Outline each uninfected red blood cell.
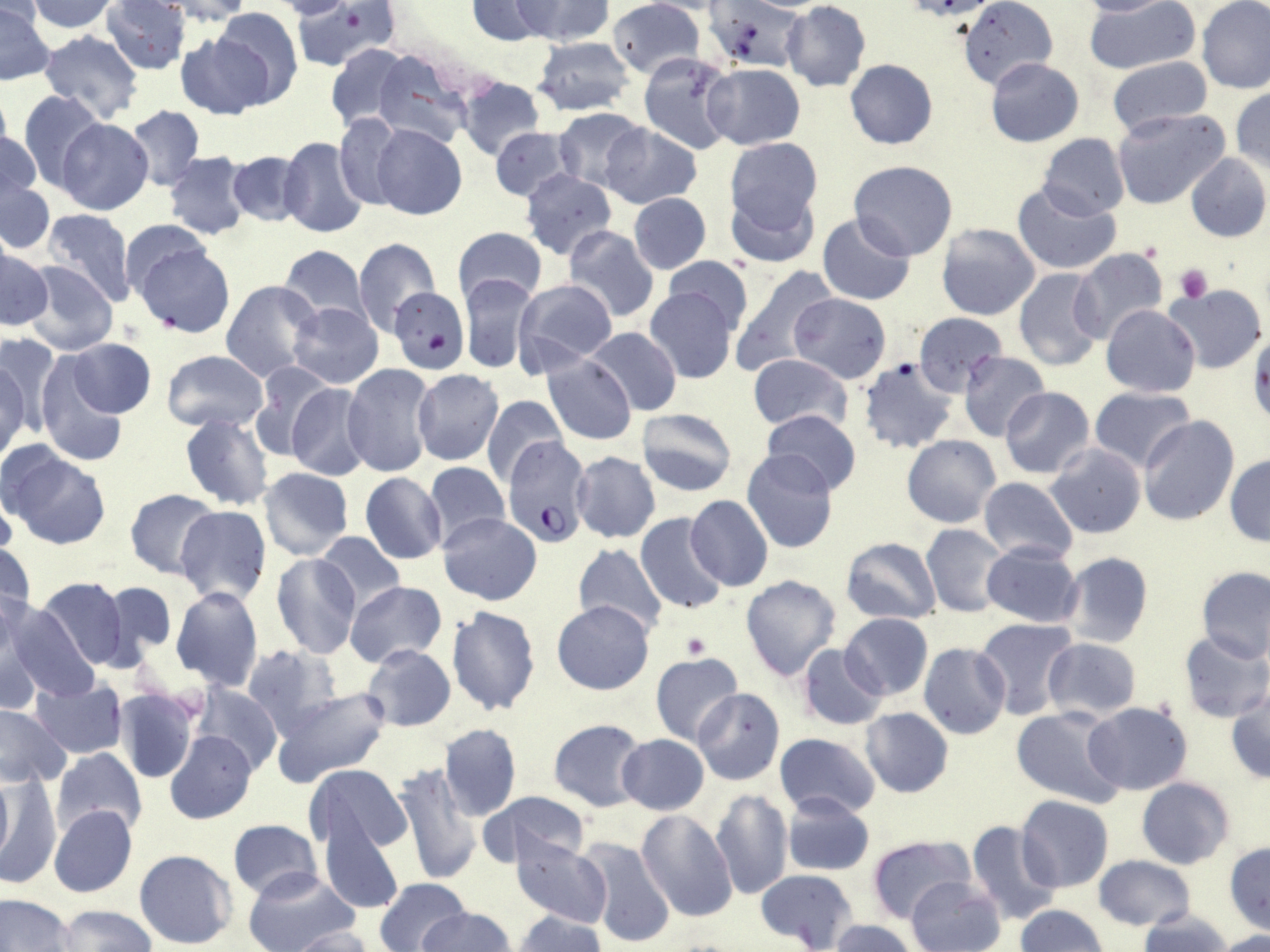
Approximate bounding boxes as (x1, y1, x2, y2) in pixels.
Uninfected red blood cells: (26, 0, 119, 35), (103, 0, 190, 74), (159, 0, 253, 25), (272, 0, 351, 20), (293, 0, 395, 72), (467, 0, 554, 45), (512, 0, 614, 45), (608, 0, 704, 78), (960, 0, 1058, 88), (1076, 0, 1171, 16), (1085, 0, 1201, 75), (1197, 0, 1270, 93), (782, 1, 871, 92), (712, 2, 804, 71), (0, 3, 54, 85), (214, 8, 303, 106), (38, 29, 145, 123), (174, 29, 274, 119), (532, 37, 636, 116), (326, 44, 412, 131), (373, 51, 477, 149), (638, 51, 737, 154), (1105, 55, 1212, 134), (985, 57, 1084, 147), (846, 59, 937, 149), (703, 64, 806, 149), (457, 77, 545, 160), (0, 86, 14, 168), (1230, 88, 1270, 176), (18, 89, 105, 189), (126, 106, 205, 191), (554, 107, 649, 194), (1112, 108, 1231, 211), (334, 115, 408, 211), (55, 117, 153, 214), (371, 123, 466, 220), (601, 124, 702, 208), (488, 126, 575, 201), (1, 129, 40, 203), (1038, 134, 1130, 219), (278, 135, 371, 239), (723, 136, 825, 242), (226, 150, 307, 226), (164, 152, 252, 237), (1185, 153, 1270, 242), (850, 161, 958, 260), (521, 170, 616, 258), (0, 179, 55, 254), (724, 180, 821, 270), (1012, 180, 1123, 275), (629, 193, 711, 273), (43, 209, 136, 305), (817, 212, 916, 305), (120, 219, 210, 302), (936, 222, 1040, 320), (563, 226, 659, 323), (453, 227, 547, 306), (353, 237, 440, 335), (135, 241, 235, 335), (278, 245, 370, 327), (1069, 247, 1167, 346), (1, 248, 53, 331), (663, 255, 754, 333), (22, 260, 118, 355), (727, 265, 839, 377), (1013, 268, 1105, 371), (457, 273, 539, 374), (221, 279, 323, 381), (513, 280, 617, 370), (1162, 285, 1268, 373), (643, 286, 739, 384), (388, 287, 468, 375), (789, 292, 890, 384), (287, 301, 384, 389), (1101, 305, 1201, 397), (912, 311, 1007, 396), (586, 327, 680, 417), (0, 339, 56, 453), (68, 339, 155, 417), (162, 350, 266, 432), (958, 350, 1050, 441), (0, 352, 31, 460), (35, 353, 130, 467), (748, 353, 854, 433), (543, 355, 637, 444), (858, 357, 958, 455), (249, 362, 334, 464), (342, 363, 435, 478), (413, 369, 503, 465), (285, 383, 374, 481), (999, 387, 1094, 478), (1090, 387, 1194, 474), (481, 395, 567, 487), (637, 407, 737, 495), (761, 411, 862, 496), (180, 413, 273, 510), (1138, 416, 1239, 526), (902, 434, 1001, 528), (1047, 443, 1146, 538), (3, 449, 111, 549), (741, 450, 838, 554), (572, 452, 661, 543), (1225, 453, 1270, 545), (422, 461, 511, 550), (258, 467, 353, 560), (360, 473, 447, 564), (977, 477, 1078, 564), (125, 489, 219, 578), (686, 494, 772, 591), (173, 505, 272, 605), (438, 512, 541, 605), (635, 512, 730, 614), (921, 524, 1011, 616), (314, 532, 407, 613), (841, 537, 943, 625), (0, 539, 35, 632), (573, 542, 667, 637), (981, 542, 1083, 627), (1060, 552, 1153, 648), (270, 553, 362, 659), (1196, 566, 1270, 661), (739, 574, 842, 682), (35, 577, 130, 671), (102, 580, 177, 660), (344, 580, 446, 669), (170, 587, 264, 692), (1, 600, 96, 702), (551, 600, 655, 695), (446, 604, 541, 716), (0, 606, 45, 713), (839, 613, 933, 701), (975, 618, 1078, 718), (1176, 632, 1270, 725), (1042, 637, 1141, 720), (919, 643, 1011, 740), (361, 644, 455, 731), (796, 644, 887, 730), (242, 645, 342, 737), (649, 652, 744, 745), (32, 678, 127, 758), (193, 683, 283, 773), (269, 684, 391, 785), (1226, 687, 1270, 786), (691, 688, 785, 785), (113, 689, 200, 783), (1082, 702, 1193, 795), (0, 704, 71, 788), (1011, 706, 1128, 808), (860, 708, 954, 797), (548, 719, 648, 811), (440, 723, 521, 820), (165, 730, 257, 824), (774, 732, 881, 817), (618, 733, 708, 814), (52, 748, 147, 839), (308, 762, 414, 865), (392, 762, 482, 886), (0, 770, 14, 871), (3, 770, 59, 891), (1136, 777, 1235, 868), (710, 789, 792, 901), (478, 791, 591, 867), (781, 791, 874, 876), (1016, 796, 1115, 893), (318, 801, 405, 917), (49, 805, 138, 898), (637, 810, 738, 922), (226, 818, 322, 898), (965, 820, 1061, 925), (512, 835, 612, 928), (866, 836, 973, 924), (578, 837, 676, 949), (1225, 842, 1270, 937), (133, 850, 238, 950), (1094, 855, 1196, 931), (244, 866, 358, 952), (756, 868, 858, 950), (907, 875, 1004, 952), (373, 876, 471, 952), (0, 895, 74, 952), (1016, 904, 1107, 952), (54, 905, 154, 952), (419, 906, 514, 951), (1138, 910, 1230, 952), (514, 911, 608, 952), (827, 920, 922, 952), (288, 926, 376, 952), (1214, 932, 1270, 952).

Summary:
  - Plasmodium falciparum-infected red blood cell locations: (502, 436, 591, 544)
  - Platelet locations: (1175, 263, 1212, 303), (1247, 333, 1270, 423), (681, 633, 709, 660)
  - Slide-level diagnosis: Plasmodium falciparum
  - Magnification: 1000x
  - Field of view: one of a larger specimen
  - Image size: 1270×952 pixels
  - Modality: light microscopy
  - Preparation: thin blood film
  - Stain: May-Grünwald-Giemsa